Give the preparation type.
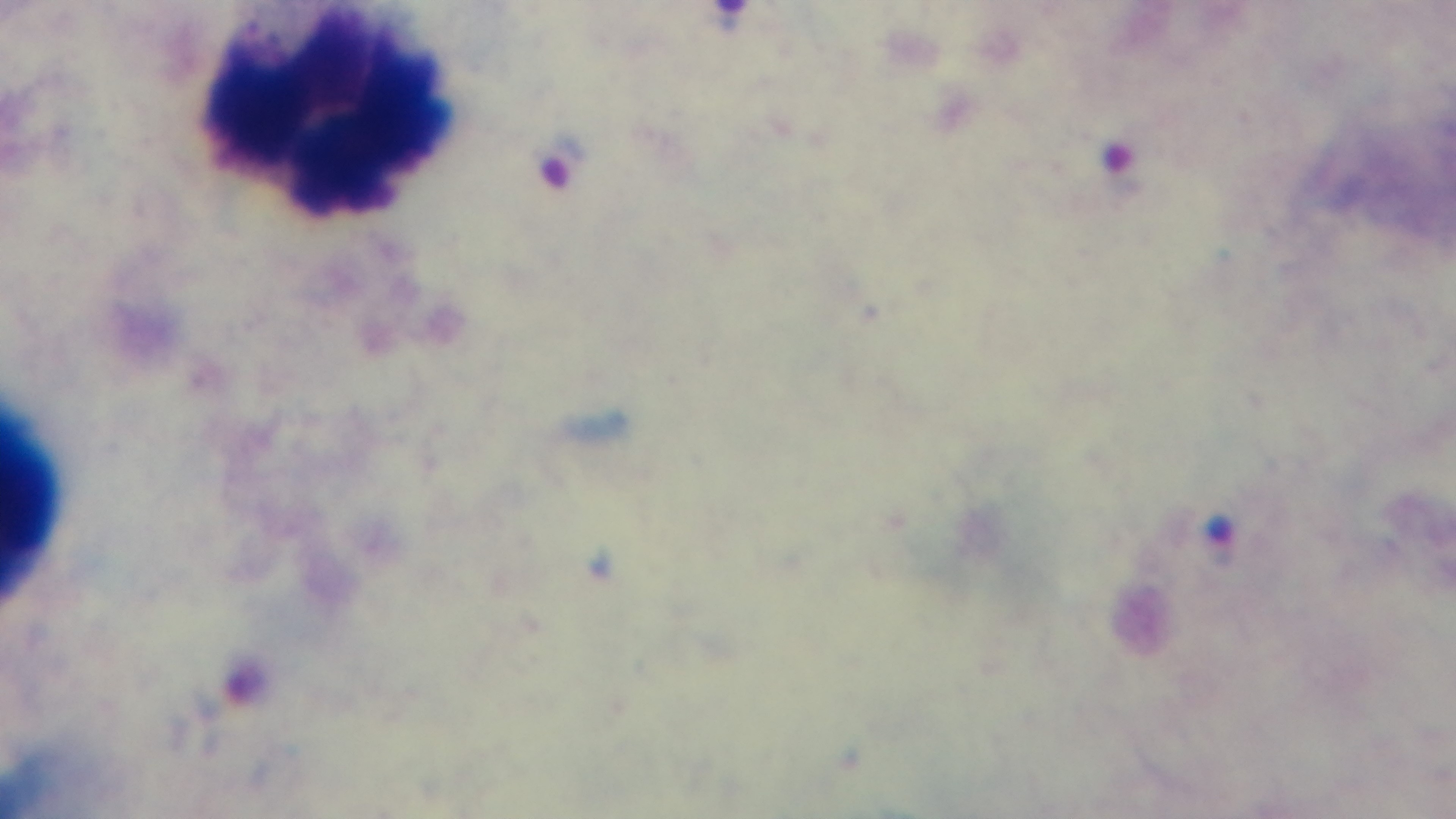

It is a thick blood film.

Oil-immersion objective, 100x. Light microscopy. Malaria status: positive. Mounted 4K digital camera. Giemsa stain. Single field of view.